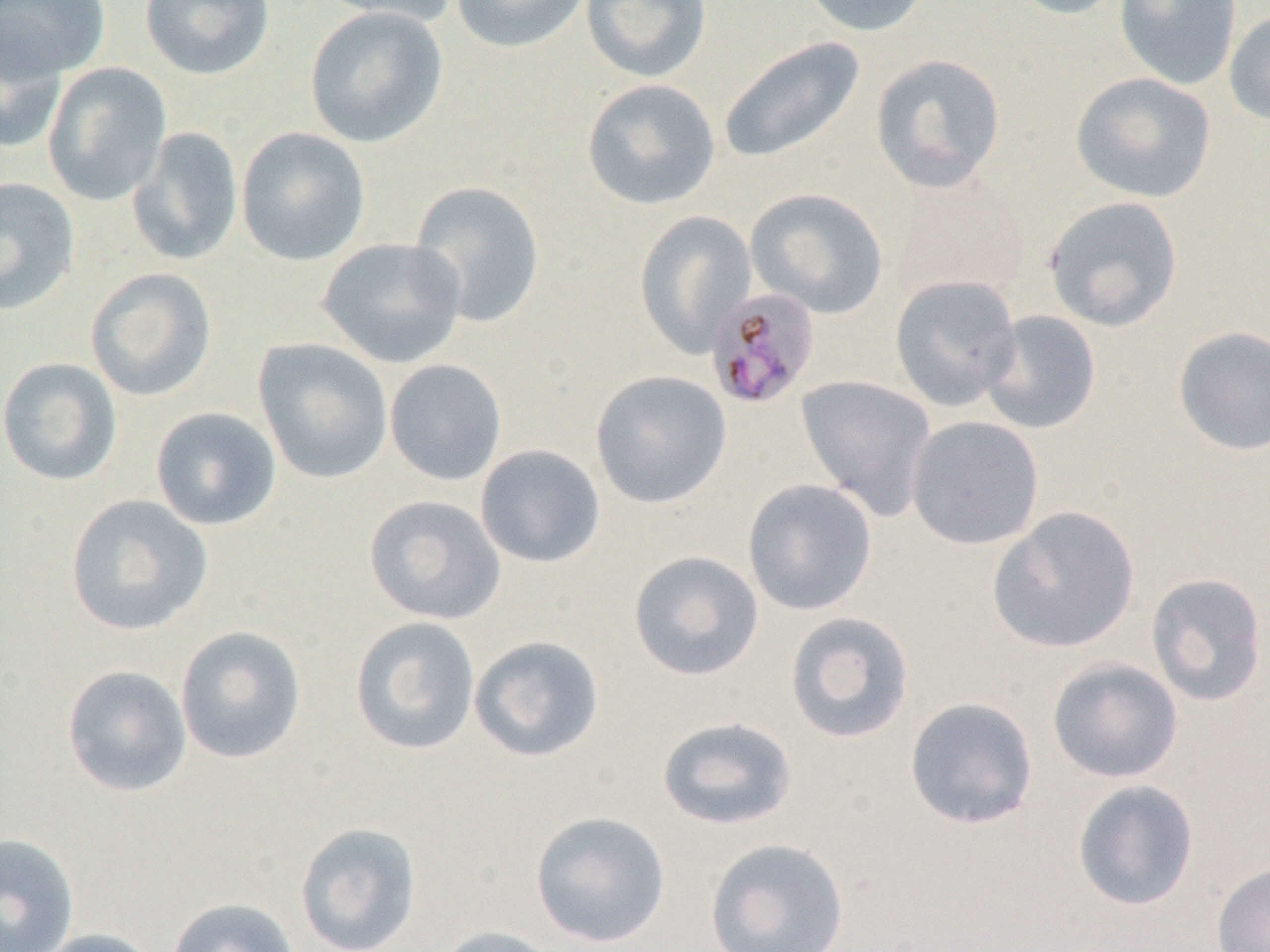
Approximate bounding boxes as [x1, y1, x2, y2] in pixels. Uninfected red blood cell locations: [1, 0, 111, 82], [139, 0, 276, 81], [313, 0, 461, 26], [450, 0, 592, 54], [580, 0, 712, 83], [798, 0, 933, 37], [1004, 0, 1132, 20], [1114, 0, 1243, 91], [304, 6, 448, 148], [1224, 8, 1270, 127], [0, 17, 70, 155], [718, 35, 865, 163], [870, 53, 1007, 193], [42, 62, 171, 205], [1071, 72, 1217, 203], [581, 78, 721, 211], [127, 126, 244, 266], [236, 126, 371, 266], [892, 167, 1030, 303], [0, 177, 80, 316], [408, 180, 546, 328], [745, 187, 889, 319], [1043, 196, 1183, 332], [634, 210, 758, 357], [316, 236, 468, 369], [85, 267, 218, 402], [890, 275, 1022, 411], [979, 309, 1101, 435], [1172, 326, 1270, 457], [253, 338, 394, 485], [0, 357, 122, 486], [384, 359, 507, 486], [591, 369, 732, 509], [796, 375, 937, 522], [150, 407, 282, 531], [906, 415, 1045, 549], [474, 444, 606, 568], [742, 478, 877, 615], [65, 494, 213, 636], [364, 494, 506, 625], [987, 505, 1140, 653], [628, 550, 765, 681], [1146, 572, 1268, 707], [784, 611, 915, 743], [350, 616, 481, 756], [175, 625, 307, 764], [468, 635, 605, 763], [1047, 657, 1183, 783], [62, 665, 192, 797], [904, 696, 1039, 830], [655, 716, 799, 830], [1071, 778, 1200, 912], [529, 810, 671, 948], [294, 822, 423, 952], [0, 832, 80, 952], [705, 837, 850, 951], [1212, 860, 1270, 952], [165, 897, 300, 952], [431, 925, 569, 952], [29, 928, 165, 952]. Plasmodium malariae-infected red blood cell locations: [704, 286, 822, 410]. Slide-level diagnosis: Plasmodium malariae. Captured at 1000x magnification. Single field of view. Light microscopy. Thin blood smear. Image is 1270×952 pixels.